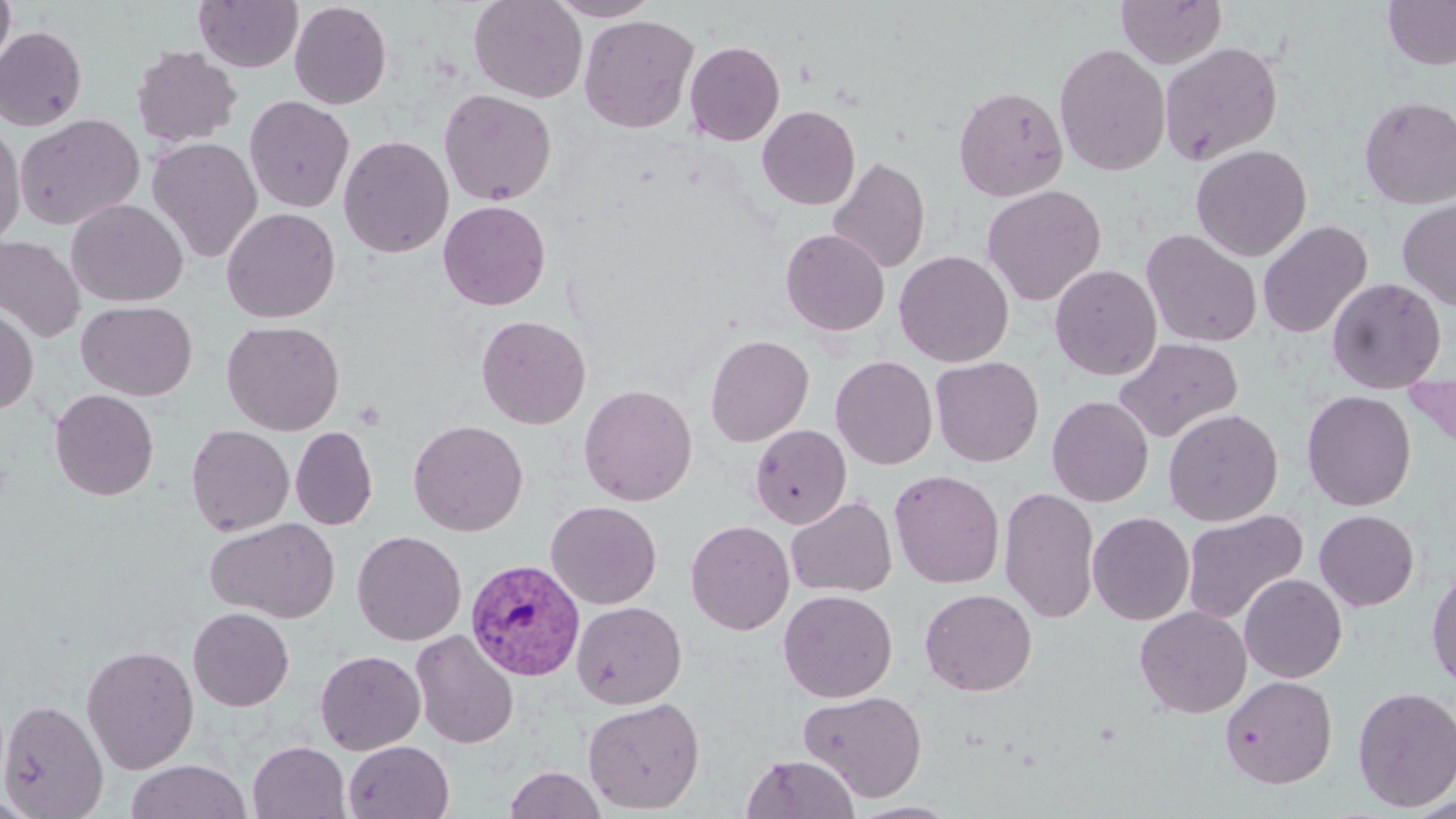

Summary:
  - Coordinate format: approximate bounding boxes as (x1,y1)-(x2,y2) corner pairs in pixels
  - Uninfected red blood cell locations: (0,0)-(16,77), (193,0)-(303,72), (468,0)-(587,103), (546,0)-(662,21), (1115,0)-(1227,69), (1382,0)-(1456,70), (289,1)-(392,109), (579,14)-(699,134), (0,26)-(87,131), (685,40)-(785,146), (1159,41)-(1284,166), (1054,43)-(1172,177), (130,45)-(242,148), (953,84)-(1069,201), (438,89)-(556,206), (244,95)-(355,213), (1358,95)-(1456,210), (757,105)-(860,210), (15,113)-(145,231), (0,121)-(26,249), (338,135)-(454,258), (148,137)-(263,263), (1191,144)-(1312,261), (827,156)-(930,274), (981,184)-(1106,306), (1397,196)-(1456,311), (66,198)-(188,306), (438,199)-(551,310), (222,207)-(340,323), (1257,219)-(1373,338), (780,228)-(890,336), (1140,228)-(1263,348), (0,236)-(84,343), (894,250)-(1014,367), (1049,264)-(1163,381), (1327,277)-(1447,394), (76,300)-(197,400), (0,304)-(38,415), (476,315)-(591,429), (222,320)-(345,435), (705,334)-(814,446), (1114,337)-(1243,442), (830,355)-(938,469), (930,356)-(1044,466), (725,362)-(829,501), (579,384)-(697,506), (50,389)-(159,501), (1301,390)-(1417,511), (1047,396)-(1154,507), (1163,408)-(1283,526), (408,419)-(529,536), (186,424)-(294,536), (750,425)-(851,529), (290,426)-(377,530), (889,469)-(1005,589), (999,486)-(1100,624), (785,495)-(897,598), (546,500)-(662,609), (1181,508)-(1308,625), (1314,509)-(1419,611), (1087,511)-(1195,625), (205,517)-(340,623), (685,519)-(795,635), (352,530)-(467,645), (1426,565)-(1456,691), (1239,573)-(1347,683), (778,589)-(897,702), (920,589)-(1037,696), (572,601)-(687,709), (1135,605)-(1252,718), (188,607)-(294,712), (410,630)-(520,749), (80,643)-(199,774), (315,650)-(426,755), (1220,675)-(1338,789), (1352,685)-(1456,812), (799,689)-(928,802), (582,697)-(705,814), (0,699)-(108,818), (247,741)-(350,819), (344,741)-(455,819), (741,753)-(860,819), (125,759)-(252,819), (504,765)-(607,819), (0,793)-(46,818), (1404,794)-(1456,818), (848,800)-(962,819)
  - Plasmodium vivax-infected red blood cell locations: (465,559)-(585,682)
  - Slide-level diagnosis: Plasmodium vivax
  - Image size: 1456×819 pixels
  - Field of view: single
  - Stain: May-Grünwald-Giemsa
  - Modality: optical microscopy
  - Preparation: thin blood smear
  - Magnification: 1000x